Name the blood parasite species.
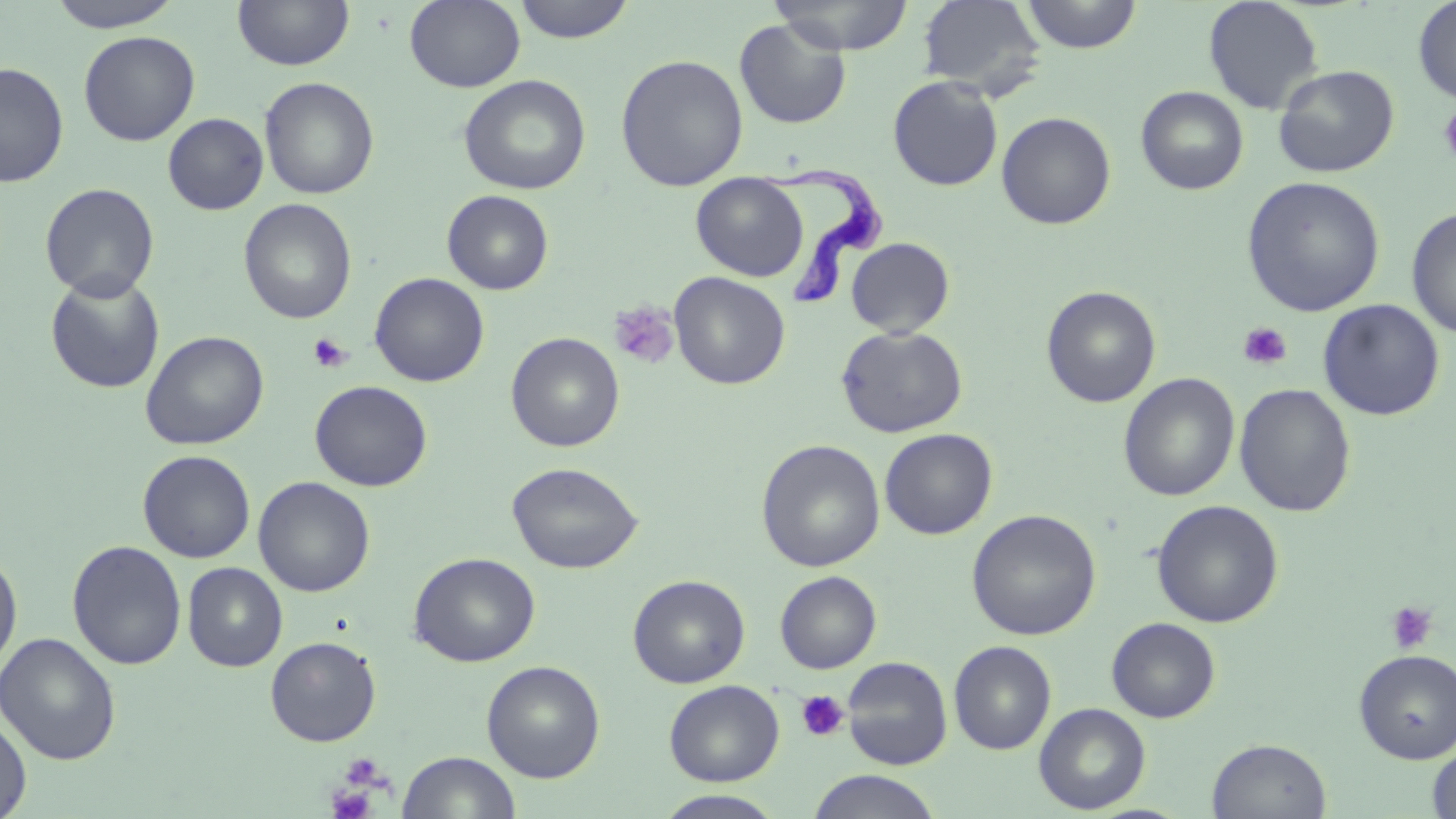

Trypanosoma brucei.

field of view = one of a larger specimen
stain = May-Grünwald-Giemsa
uninfected red blood cell locations = approximate bounding boxes as [x1, y1, x2, y2] in pixels: [46, 0, 184, 32], [232, 0, 355, 70], [404, 0, 525, 92], [512, 0, 636, 44], [768, 0, 915, 55], [917, 0, 1047, 97], [1019, 0, 1143, 53], [1203, 0, 1324, 115], [1412, 0, 1456, 105], [734, 18, 852, 130], [79, 30, 200, 146], [615, 54, 749, 191], [0, 62, 69, 187], [1272, 64, 1400, 178], [458, 74, 591, 195], [887, 76, 1004, 191], [259, 77, 379, 200], [1136, 86, 1248, 195], [996, 111, 1116, 230], [163, 113, 269, 215], [691, 173, 807, 282], [1242, 176, 1385, 317], [39, 183, 159, 302], [442, 190, 554, 294], [238, 198, 357, 324], [1406, 207, 1456, 339], [846, 237, 955, 338], [44, 271, 166, 394], [669, 271, 790, 390], [370, 272, 489, 387], [1041, 286, 1162, 408], [1318, 299, 1445, 421], [836, 325, 968, 438], [140, 330, 269, 450], [505, 332, 625, 452], [1118, 373, 1239, 502], [309, 380, 433, 491], [1233, 383, 1356, 517], [879, 428, 998, 540], [756, 440, 885, 572], [138, 450, 255, 562], [507, 461, 644, 574], [253, 476, 375, 597], [1151, 499, 1284, 628], [966, 509, 1102, 641], [67, 540, 187, 670], [0, 549, 23, 675], [408, 552, 541, 667], [182, 562, 287, 671], [775, 571, 881, 674], [628, 575, 750, 688], [1106, 617, 1220, 723], [0, 632, 121, 765], [265, 636, 381, 746], [949, 641, 1056, 754], [1353, 649, 1456, 763], [841, 656, 953, 770], [481, 660, 606, 783], [664, 680, 784, 786], [1034, 702, 1151, 814], [0, 714, 32, 818], [1207, 737, 1332, 819], [1426, 742, 1456, 818], [397, 750, 521, 818], [805, 770, 943, 819], [652, 790, 788, 818]
magnification = 1000x
platelet locations = approximate bounding boxes as [x1, y1, x2, y2] in pixels: [1438, 105, 1456, 165], [610, 302, 680, 370], [1238, 322, 1292, 370], [307, 333, 352, 374], [1385, 600, 1438, 655], [796, 690, 850, 742], [338, 753, 388, 791], [326, 785, 377, 819]
preparation = thin blood smear
Trypanosoma brucei locations = approximate bounding boxes as [x1, y1, x2, y2] in pixels: [759, 159, 887, 306]
modality = optical microscopy
image size = 1456×819 pixels